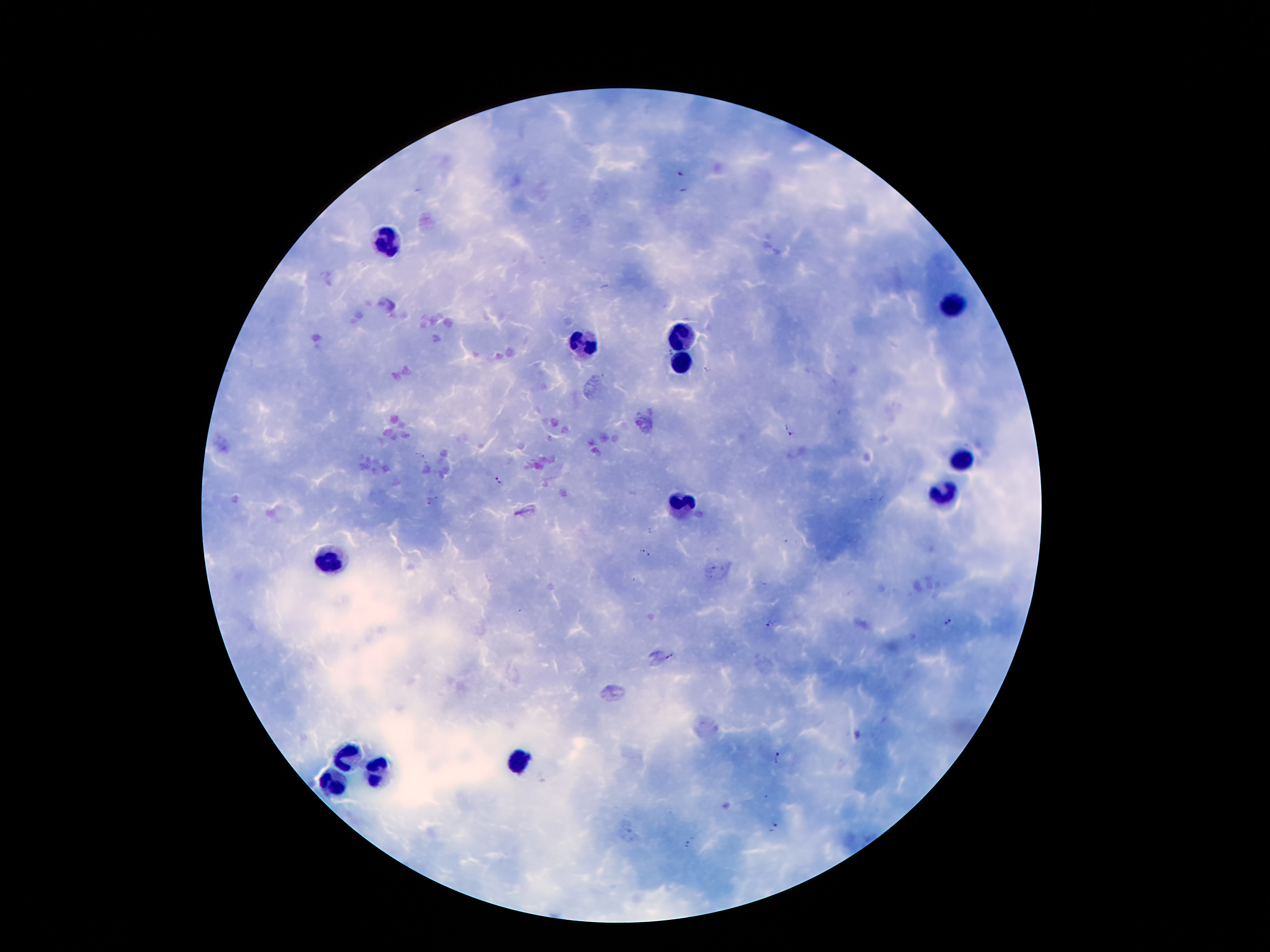 Approximate centers as {x, y} in pixels. Leukocyte locations: {385, 239}, {954, 306}, {679, 335}, {586, 346}, {681, 363}, {962, 463}, {945, 497}, {685, 508}, {326, 562}, {349, 757}, {517, 760}, {376, 776}, {334, 783}. Plasmodium parasite locations: {680, 173}, {682, 191}, {670, 352}, {707, 369}, {787, 431}, {419, 456}, {498, 481}, {430, 502}, {649, 532}, {645, 553}, {948, 622}, {771, 624}, {670, 656}, {776, 757}, {774, 829}, {690, 842}. One field from this slide. Patient malaria status: infected with Plasmodium falciparum. 100x magnification. Giemsa stain. Thick blood film. Smartphone photograph taken through the microscope eyepiece. Image is 1270×952 pixels.